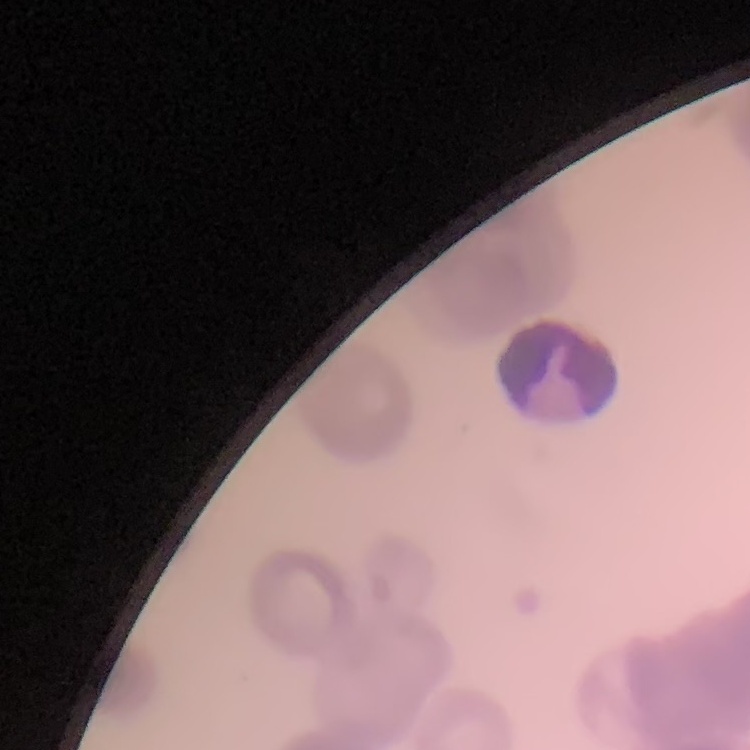
The red blood cells show rouleaux formation. Stained with either Field's or Giemsa. Thin blood film. Square crop of a larger photomicrograph.